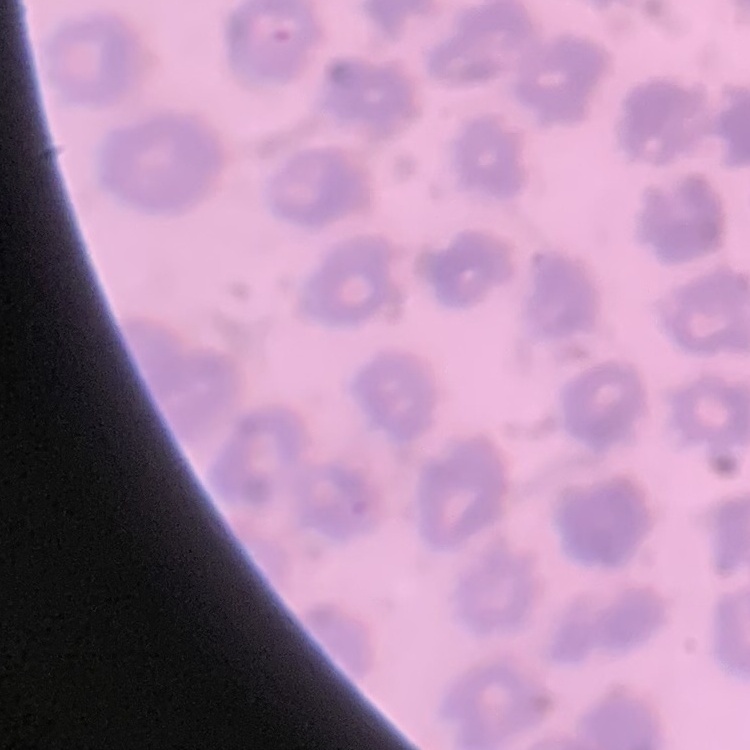
Summary:
  - Red blood cell morphology: no rouleaux formation
  - Preparation: thin blood smear
  - Stain: Field's or Giemsa
  - Image type: one tile cut from a larger photomicrograph